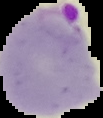

Summary:
  - Preparation: thin blood film
  - Image size: 103×118 pixels
  - Image type: segmented cell region with the area outside set to black
  - Malaria status: parasitized